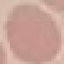

Malaria status: uninfected. Thin blood film. Automatically extracted cell patch, resized to 64 × 64 pixels. Photographed with a smartphone camera at the microscope eyepiece. Giemsa-stained preparation.